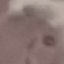 Result: malaria parasites detected. Photographed with a smartphone camera at the microscope eyepiece. Automatically extracted cell patch, resized to 64 × 64 pixels. Thin smear of blood. Giemsa-stained preparation.